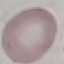

result = no malaria parasites detected
preparation = thin blood smear
stain = Giemsa
capture = smartphone through the microscope eyepiece
image type = automatically extracted cell patch, resized to 64 × 64 pixels